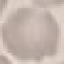

Result: no malaria parasites detected. Giemsa stain. Photographed with a smartphone camera at the microscope eyepiece. Thin blood smear. Automatically extracted cell patch, resized to 64 × 64 pixels.